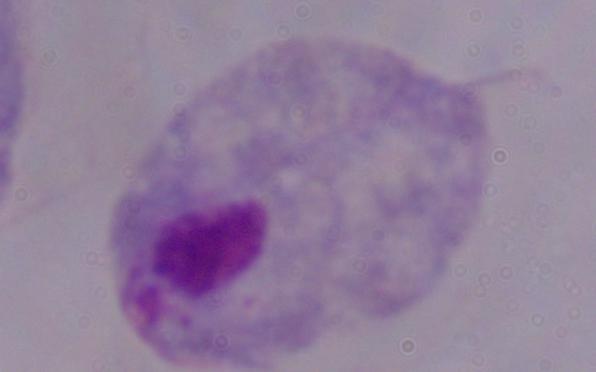

A trichomonad is seen. Captured at 1000x magnification. Micrograph.